Identify the blood parasite species.
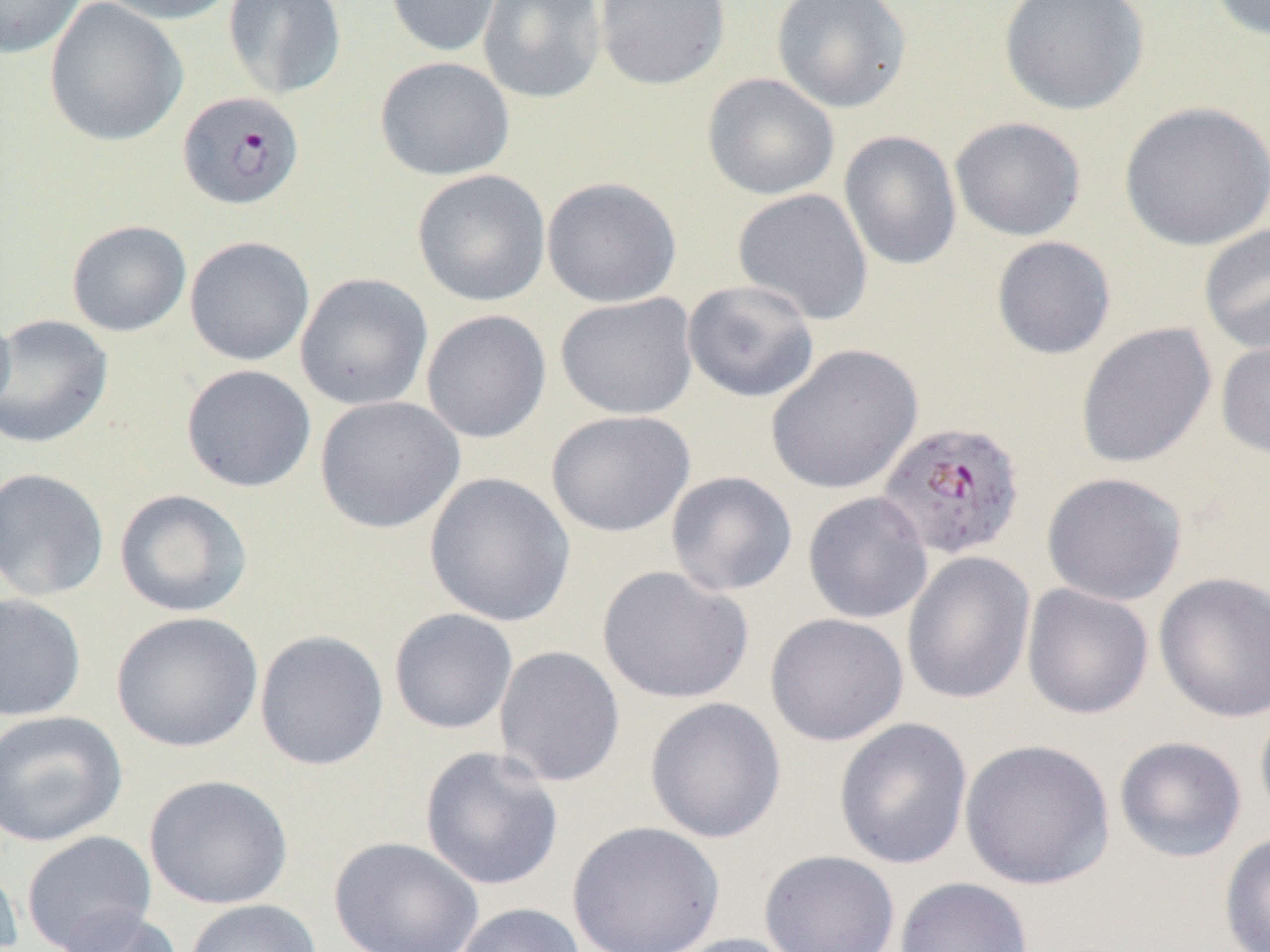

Plasmodium falciparum.

Approximate bounding boxes as (x1, y1, x2, y2) in pixels. Uninfected red blood cell locations: (0, 0, 85, 58), (44, 0, 188, 147), (95, 0, 240, 25), (223, 0, 347, 101), (385, 0, 503, 58), (478, 0, 606, 104), (594, 0, 731, 91), (771, 0, 913, 114), (998, 0, 1150, 116), (1207, 0, 1269, 41), (374, 55, 515, 181), (701, 73, 840, 201), (1118, 101, 1270, 252), (949, 117, 1087, 241), (839, 130, 962, 272), (412, 169, 551, 306), (541, 176, 682, 308), (732, 188, 874, 326), (66, 220, 191, 337), (1198, 223, 1270, 354), (184, 235, 315, 367), (991, 235, 1116, 360), (295, 272, 433, 411), (682, 279, 820, 403), (554, 293, 699, 419), (0, 306, 15, 421), (421, 309, 552, 444), (0, 313, 114, 450), (1075, 321, 1217, 469), (1215, 335, 1270, 460), (765, 343, 923, 494), (180, 364, 316, 493), (314, 395, 465, 534), (546, 410, 695, 537), (0, 467, 110, 602), (665, 470, 798, 597), (1042, 471, 1187, 605), (423, 472, 576, 627), (114, 488, 253, 617), (802, 490, 933, 624), (901, 551, 1036, 705), (596, 565, 754, 704), (1154, 571, 1270, 723), (1021, 583, 1154, 719), (0, 591, 87, 722), (388, 608, 518, 735), (110, 611, 264, 753), (765, 612, 908, 746), (254, 630, 389, 771), (494, 645, 626, 788), (644, 696, 787, 843), (1254, 700, 1270, 829), (0, 709, 128, 848), (833, 717, 973, 870), (1113, 735, 1247, 862), (960, 738, 1114, 891), (419, 746, 564, 891), (144, 774, 293, 910), (565, 820, 725, 952), (21, 831, 156, 951), (1218, 831, 1270, 952), (328, 835, 484, 952), (759, 849, 900, 952), (0, 857, 23, 951), (894, 876, 1034, 952), (184, 898, 322, 952), (453, 902, 586, 952), (56, 906, 183, 952), (666, 933, 806, 952). Plasmodium falciparum-infected red blood cell locations: (176, 90, 305, 210), (877, 424, 1027, 565). Thin blood smear. One field of a larger specimen. Light microscopy. Captured at 1000x magnification. Image is 1270×952 pixels.